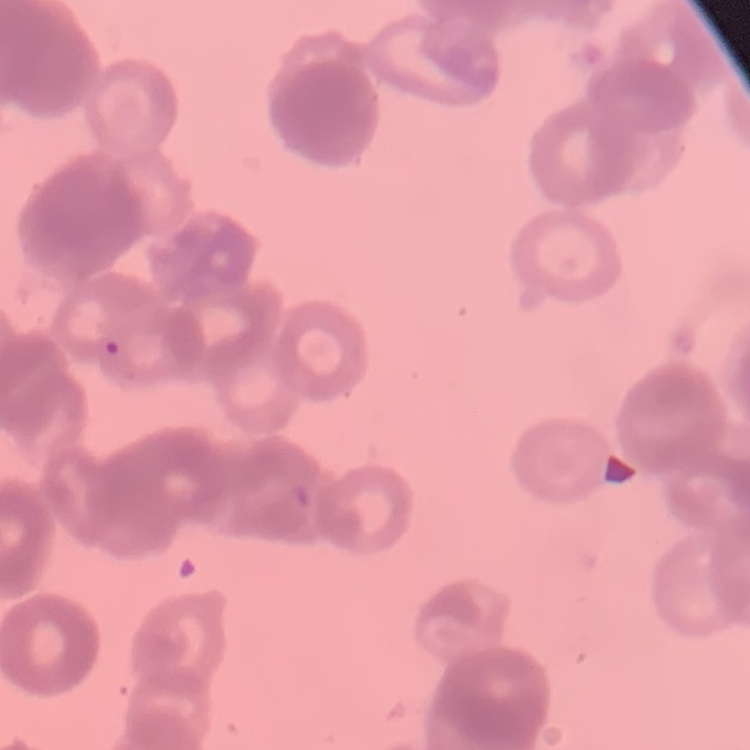
Summary:
  - Erythrocyte morphology: rouleaux formation
  - Stain: Field's or Giemsa
  - Preparation: thin blood film
  - Image type: square crop of a larger photomicrograph